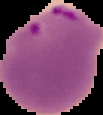

Summary:
  - Preparation: thin blood smear
  - Malaria status: parasitized
  - Image type: segmented cell region on a black background
  - Image size: 103×115 pixels